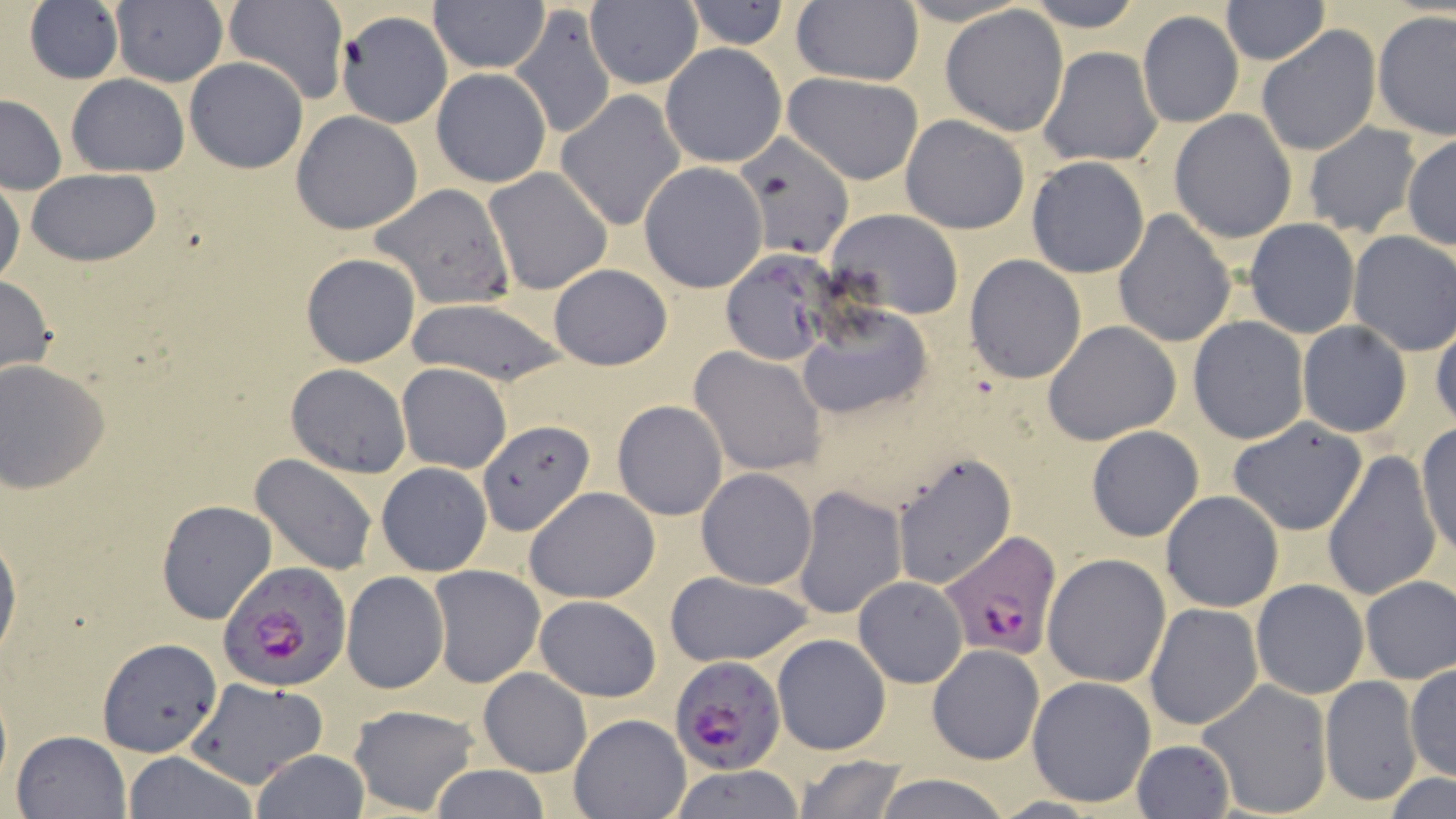

slide-level diagnosis = Plasmodium falciparum
magnification = 1000x
Plasmodium falciparum-infected red blood cell locations = approximate bounding boxes as (x1, y1, x2, y2) in pixels: (939, 529, 1063, 659), (218, 561, 352, 694), (668, 653, 786, 776)
stain = May-Grünwald-Giemsa
preparation = thin blood smear
uninfected red blood cell locations = approximate bounding boxes as (x1, y1, x2, y2) in pixels: (223, 0, 349, 105), (427, 0, 548, 72), (791, 0, 924, 88), (1022, 0, 1148, 30), (22, 1, 126, 85), (109, 1, 228, 88), (584, 1, 701, 90), (681, 1, 792, 50), (1221, 1, 1329, 64), (508, 3, 616, 141), (941, 5, 1071, 136), (1136, 10, 1244, 129), (1373, 11, 1455, 139), (336, 12, 452, 128), (1255, 25, 1381, 157), (660, 42, 787, 168), (1036, 46, 1163, 167), (184, 57, 308, 173), (430, 67, 553, 188), (783, 71, 926, 184), (67, 74, 190, 176), (556, 90, 685, 232), (0, 94, 67, 192), (1168, 109, 1298, 244), (291, 110, 423, 233), (901, 115, 1029, 235), (1301, 123, 1422, 238), (731, 130, 854, 259), (1402, 136, 1456, 250), (1025, 155, 1150, 278), (639, 162, 767, 293), (484, 166, 613, 295), (25, 170, 162, 266), (0, 179, 24, 290), (371, 183, 516, 310), (826, 209, 965, 320), (1111, 209, 1237, 347), (1244, 219, 1361, 337), (1347, 231, 1456, 355), (722, 250, 835, 365), (300, 252, 422, 368), (964, 255, 1086, 383), (548, 263, 673, 369), (0, 272, 56, 380), (402, 298, 572, 389), (797, 303, 934, 420), (1431, 313, 1456, 430), (1188, 316, 1308, 444), (1044, 321, 1182, 444), (1297, 321, 1412, 437), (689, 346, 826, 476), (0, 359, 110, 495), (396, 362, 512, 473), (286, 364, 411, 476), (613, 399, 728, 521), (1226, 416, 1371, 535), (478, 418, 594, 536), (1415, 421, 1454, 559), (1086, 425, 1204, 541), (1320, 447, 1441, 604), (891, 449, 1017, 589), (250, 454, 379, 576), (375, 461, 493, 574), (698, 468, 817, 588), (793, 485, 906, 620), (525, 487, 659, 604), (1160, 490, 1284, 612), (155, 499, 278, 626), (0, 525, 21, 669), (1042, 554, 1170, 688), (430, 566, 544, 686), (340, 571, 451, 694), (661, 571, 816, 669), (854, 576, 968, 687), (1359, 576, 1455, 683), (1250, 579, 1369, 700), (535, 596, 661, 703), (1144, 603, 1263, 732), (772, 633, 891, 755), (97, 637, 221, 756), (927, 644, 1044, 764), (1405, 662, 1455, 783), (478, 667, 591, 777), (1026, 676, 1156, 808), (1320, 676, 1422, 805), (186, 677, 329, 788), (1197, 677, 1334, 818), (348, 703, 480, 815), (569, 712, 690, 819), (11, 730, 130, 819), (1130, 738, 1235, 818), (251, 748, 369, 819), (122, 751, 259, 819), (791, 755, 910, 819), (428, 765, 552, 819), (663, 766, 806, 819), (869, 772, 1014, 819), (1383, 774, 1456, 819)
field of view = one of a larger specimen
image size = 1456×819 pixels
modality = light microscopy